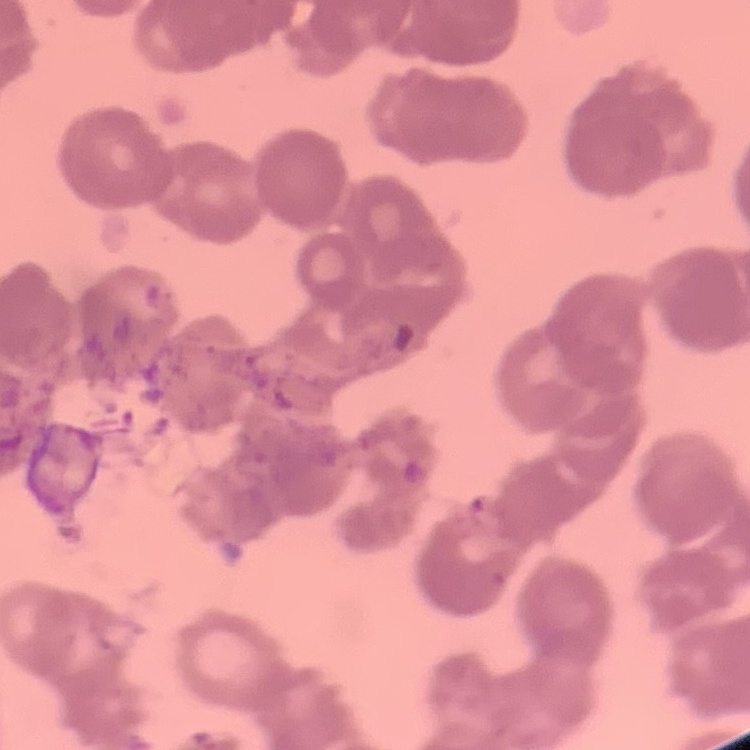

The erythrocytes exhibit rouleaux formation. Thin peripheral smear. Square crop of a larger photomicrograph. Field's or Giemsa stain.